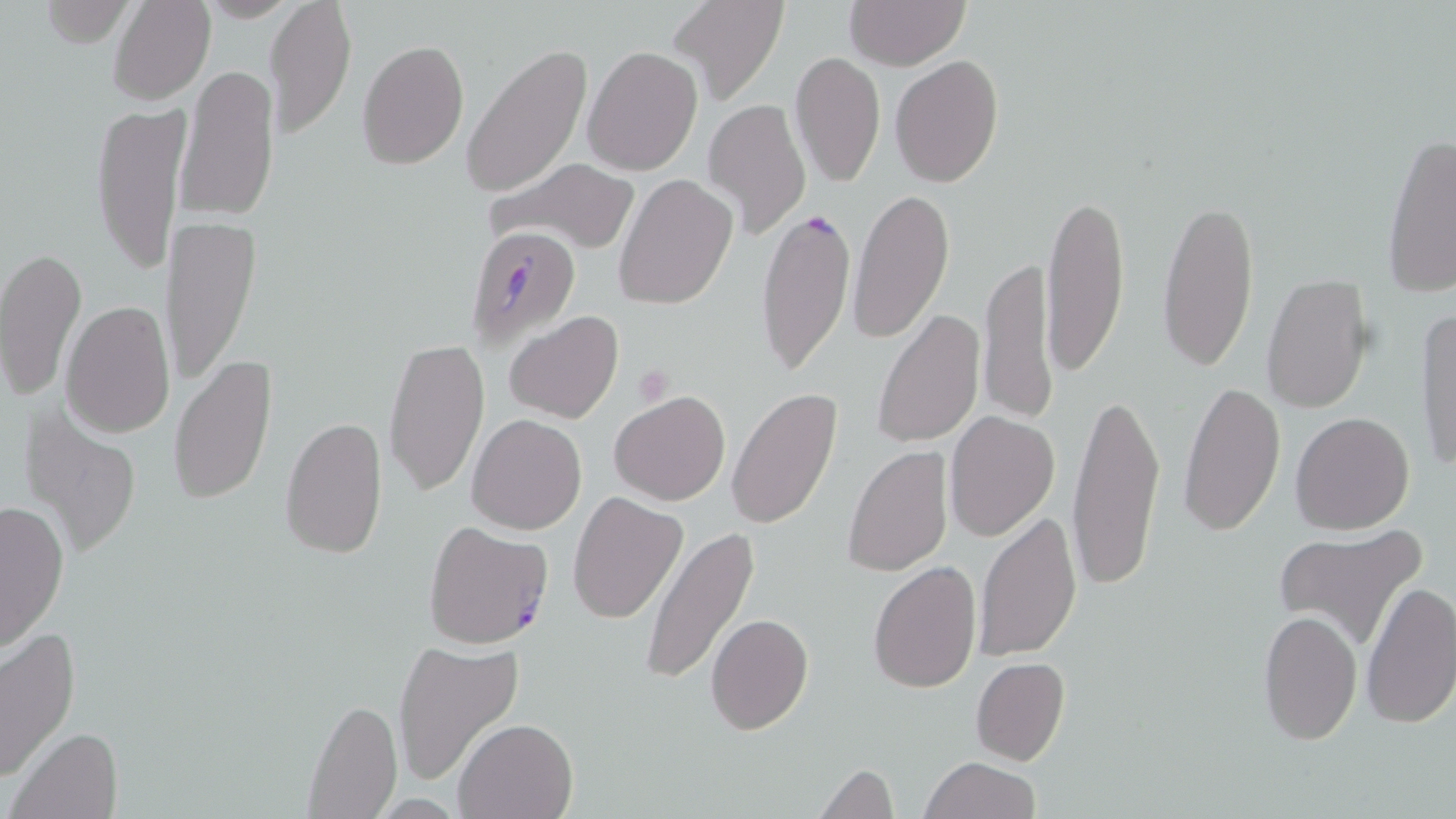 Approximate bounding boxes as (x1, y1, x2, y2) in pixels. Platelet locations: (634, 366, 671, 406). Uninfected red blood cell locations: (108, 0, 215, 105), (265, 0, 357, 139), (669, 0, 787, 108), (843, 0, 970, 70), (25, 1, 144, 47), (355, 40, 469, 169), (461, 43, 591, 197), (583, 44, 703, 176), (790, 50, 886, 186), (889, 55, 1004, 188), (176, 64, 280, 221), (704, 98, 812, 239), (92, 100, 190, 276), (1380, 132, 1456, 298), (485, 157, 641, 256), (613, 174, 738, 310), (849, 187, 955, 345), (1042, 192, 1130, 377), (1157, 195, 1261, 373), (162, 215, 261, 385), (1, 247, 87, 402), (979, 253, 1056, 426), (1261, 273, 1375, 413), (61, 298, 175, 438), (1415, 307, 1456, 474), (870, 308, 986, 450), (504, 311, 623, 425), (382, 335, 488, 498), (169, 352, 279, 507), (1177, 380, 1287, 536), (1067, 384, 1165, 596), (726, 388, 843, 531), (609, 390, 730, 505), (19, 407, 144, 561), (944, 411, 1061, 542), (1290, 411, 1415, 535), (279, 414, 388, 560), (466, 414, 587, 534), (842, 446, 954, 577), (568, 491, 688, 625), (0, 499, 70, 650), (973, 509, 1082, 663), (1273, 523, 1428, 651), (639, 526, 760, 683), (868, 561, 982, 692), (1361, 580, 1456, 730), (1256, 607, 1364, 746), (705, 613, 814, 734), (0, 627, 80, 785), (391, 638, 526, 787), (971, 656, 1071, 767), (303, 697, 401, 817), (454, 717, 579, 819), (9, 726, 123, 819), (920, 756, 1039, 819), (814, 763, 897, 818). Plasmodium falciparum-infected red blood cell locations: (756, 205, 856, 375), (462, 226, 580, 351), (422, 521, 551, 650). Slide-level diagnosis: Plasmodium falciparum. Light microscopy. Thin blood smear. Image is 1456×819 pixels. One field of a larger specimen. 1000x magnification. May-Grünwald-Giemsa-stained preparation.